Assess this cell for malaria.
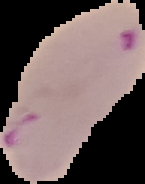

It is parasitized.

Summary:
  - Image size: 145×184 pixels
  - Preparation: thin blood smear
  - Image type: segmented cell region on a black background